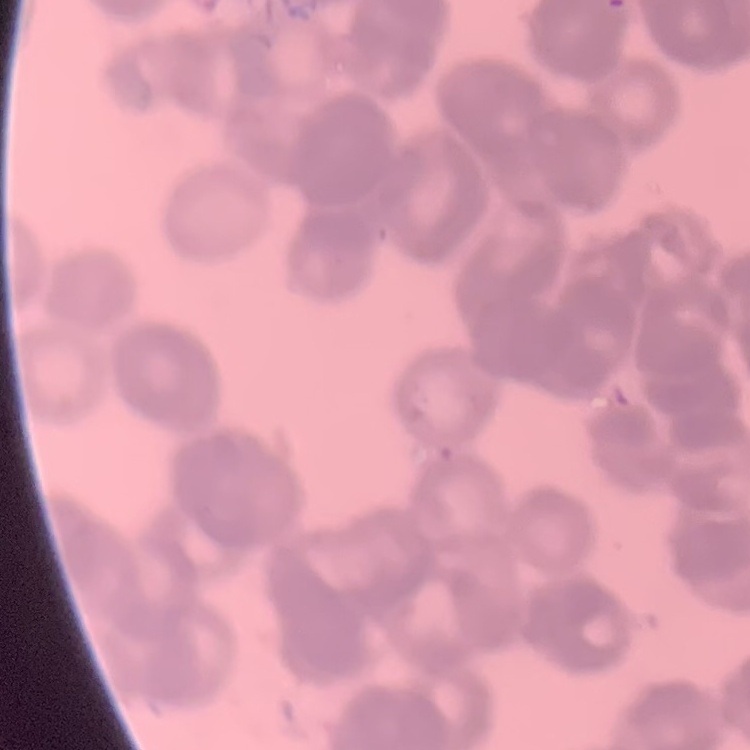

The erythrocytes exhibit rouleaux formation. Square crop of a larger photomicrograph. Field's or Giemsa stain. Thin peripheral smear.